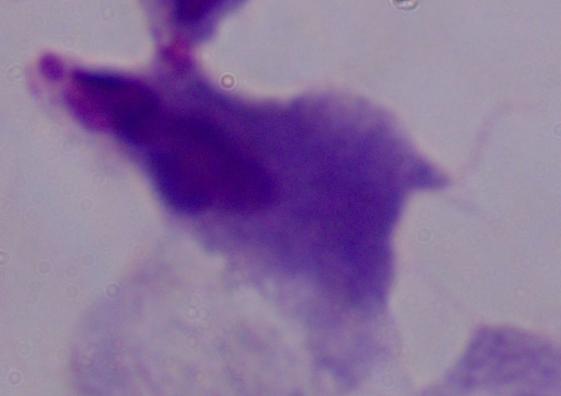
magnification = 1000x
identification = trichomonad
modality = micrograph